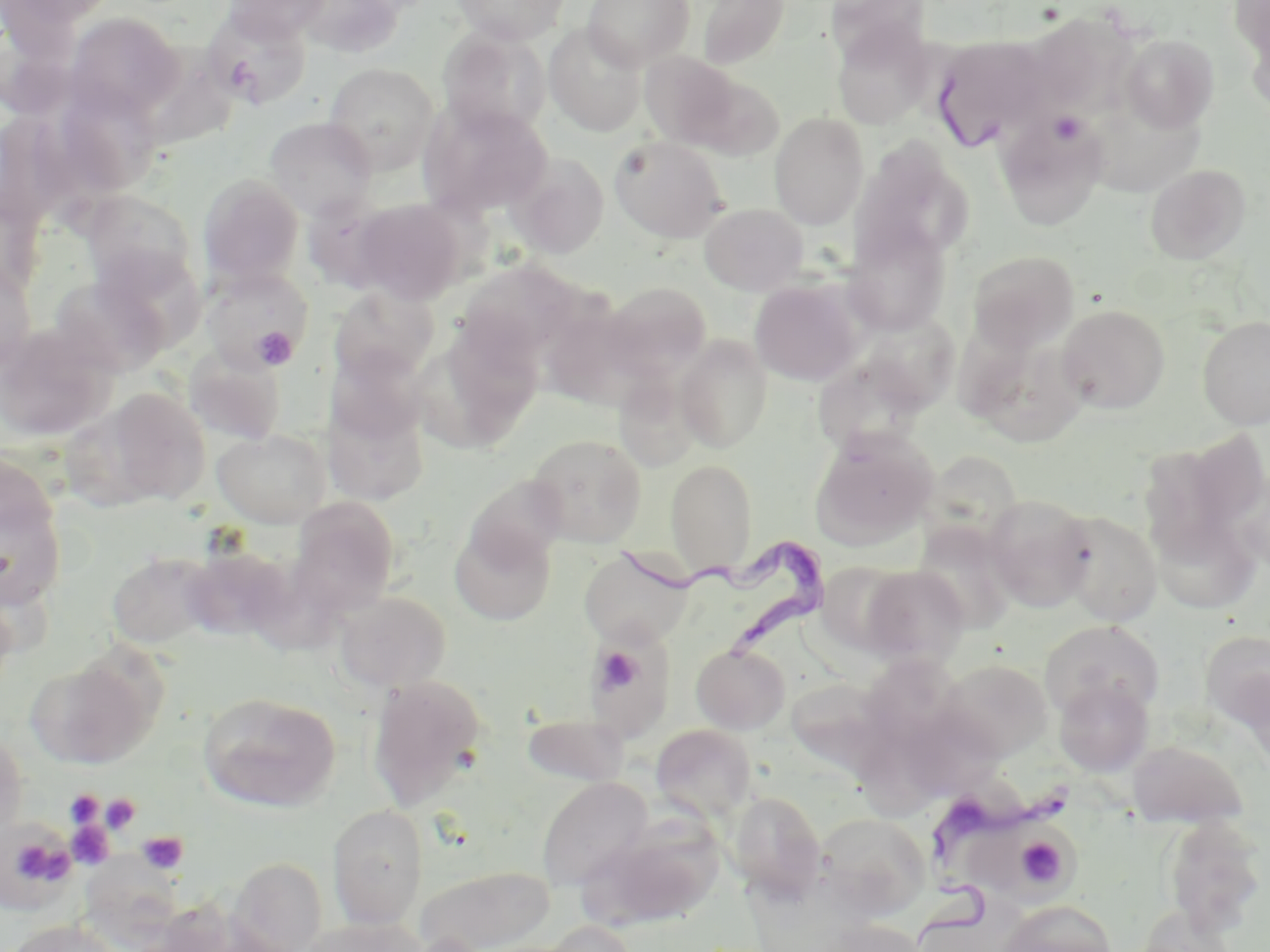
Summary:
  - Coordinate format: approximate bounding boxes as (x1, y1, x2, y2) in pixels
  - Uninfected red blood cell locations: (0, 0, 116, 35), (221, 0, 332, 45), (293, 0, 405, 59), (451, 0, 569, 45), (582, 0, 695, 69), (696, 0, 789, 69), (825, 0, 929, 63), (1232, 0, 1270, 90), (202, 9, 312, 109), (1026, 11, 1138, 116), (64, 12, 183, 120), (544, 23, 647, 136), (832, 25, 933, 128), (439, 29, 551, 137), (1120, 34, 1219, 132), (931, 36, 1053, 151), (640, 51, 742, 149), (323, 63, 439, 175), (688, 74, 785, 162), (67, 94, 163, 190), (418, 100, 553, 218), (1084, 106, 1206, 201), (996, 110, 1108, 230), (769, 112, 869, 229), (265, 117, 377, 220), (609, 135, 728, 243), (850, 141, 972, 268), (507, 152, 609, 259), (1146, 164, 1251, 264), (198, 174, 304, 287), (79, 191, 200, 296), (303, 192, 405, 292), (352, 199, 467, 304), (700, 203, 808, 295), (843, 220, 952, 336), (89, 243, 207, 353), (967, 250, 1080, 354), (458, 260, 584, 370), (0, 262, 36, 377), (200, 267, 314, 374), (50, 273, 173, 377), (749, 279, 863, 386), (601, 281, 712, 382), (328, 286, 439, 385), (538, 299, 643, 407), (1057, 304, 1171, 414), (856, 313, 963, 415), (1198, 314, 1270, 429), (421, 319, 546, 451), (0, 323, 116, 443), (961, 331, 1087, 447), (674, 336, 774, 452), (325, 344, 429, 446), (183, 348, 286, 446), (812, 354, 931, 457), (612, 370, 703, 473), (322, 384, 430, 507), (96, 388, 211, 508), (213, 429, 331, 528), (811, 429, 937, 548), (1186, 430, 1270, 537), (527, 434, 647, 547), (922, 450, 1025, 551), (666, 459, 757, 577), (0, 466, 67, 611), (1232, 467, 1270, 574), (984, 495, 1095, 613), (287, 497, 401, 616), (1057, 510, 1163, 626), (1149, 515, 1261, 614), (449, 522, 556, 626), (912, 523, 1018, 633), (181, 546, 294, 643), (578, 547, 695, 647), (106, 552, 220, 649), (817, 561, 912, 654), (859, 565, 970, 667), (0, 585, 19, 705), (334, 591, 451, 692), (1040, 620, 1165, 721), (1200, 630, 1270, 728), (692, 643, 790, 734), (586, 648, 676, 742), (28, 655, 160, 771), (861, 657, 973, 748), (938, 659, 1053, 761), (1236, 668, 1270, 775), (367, 675, 489, 808), (1054, 679, 1153, 777), (789, 680, 902, 782), (198, 692, 341, 813), (859, 709, 973, 812), (522, 713, 629, 787), (651, 723, 757, 823), (0, 726, 28, 844), (1128, 740, 1248, 829), (536, 776, 653, 891), (727, 790, 826, 899), (327, 804, 429, 929), (816, 813, 930, 919), (581, 816, 724, 932), (1162, 816, 1267, 936), (970, 824, 1084, 906), (79, 851, 186, 949), (229, 857, 327, 952), (416, 864, 555, 952), (998, 901, 1117, 952), (1133, 906, 1237, 951), (300, 917, 424, 952), (4, 919, 123, 952), (816, 919, 928, 952), (541, 920, 639, 952)
  - Platelet locations: (1049, 111, 1086, 146), (251, 326, 298, 369), (595, 646, 647, 696), (64, 789, 104, 828), (99, 793, 141, 834), (65, 819, 115, 870), (1, 831, 75, 901), (136, 831, 188, 875), (1014, 835, 1070, 890)
  - Trypanosoma brucei locations: (615, 531, 830, 662), (918, 783, 1074, 940)
  - Slide-level diagnosis: Trypanosoma brucei
  - Field of view: one of a larger specimen
  - Magnification: 1000x
  - Stain: May-Grünwald-Giemsa
  - Image size: 1270×952 pixels
  - Modality: optical microscopy
  - Preparation: thin blood film